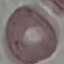

{
  "malaria_status": "uninfected",
  "preparation": "thin smear",
  "capture": "smartphone camera at the microscope eyepiece",
  "image_type": "cell patch, automatically extracted from a larger field of view and resized to 64 × 64 pixels",
  "stain": "Giemsa"
}